State the preparation type.
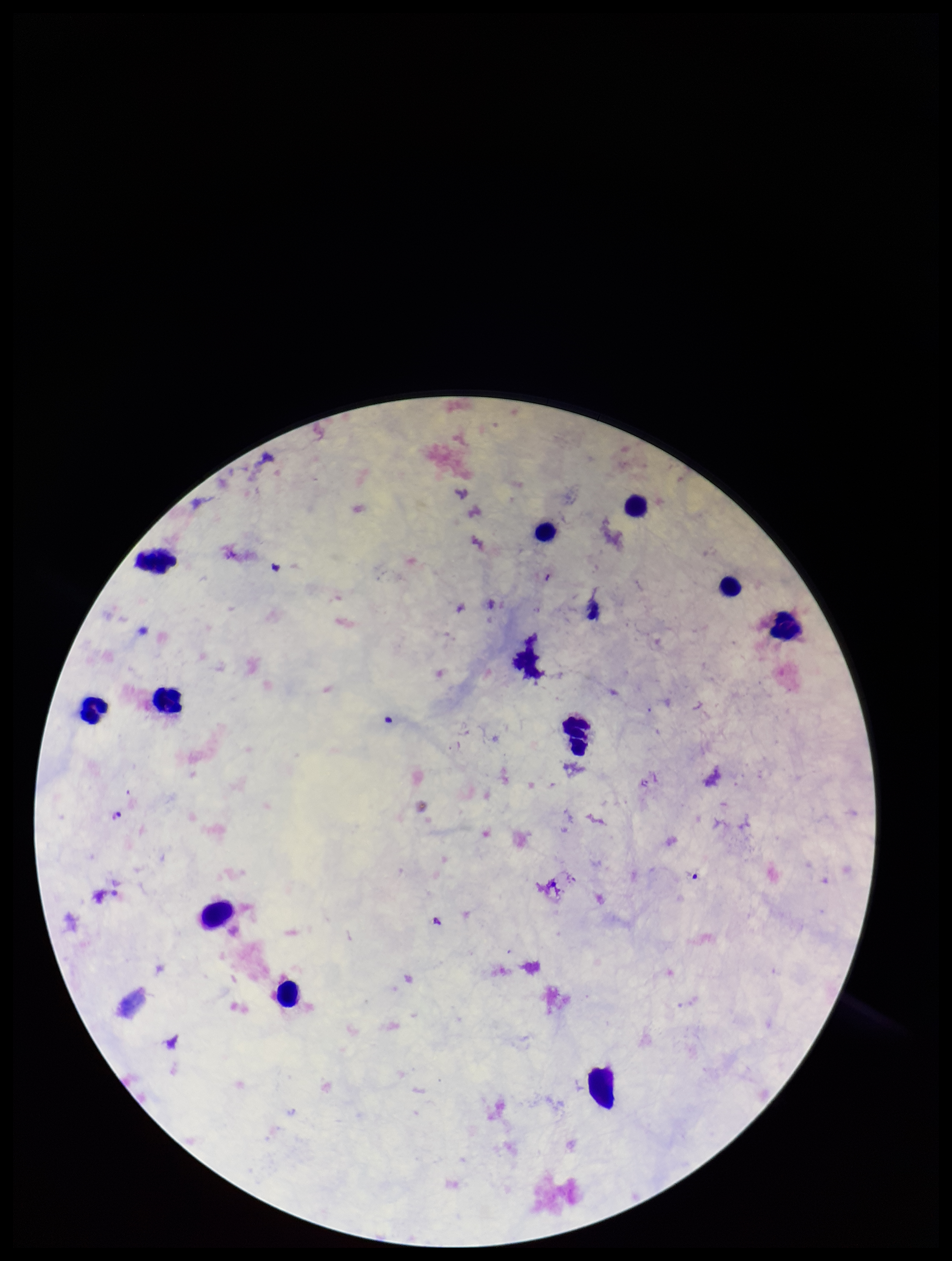

A thick smear.

Summary:
  - Leukocyte count: 12
  - Image size: 952×1261 pixels
  - Parasite count: 0
  - Capture: smartphone photograph through the microscope eyepiece
  - Patient malaria status: negative
  - Plasmodium parasites: none identified
  - Stain: Giemsa
  - Field of view: single